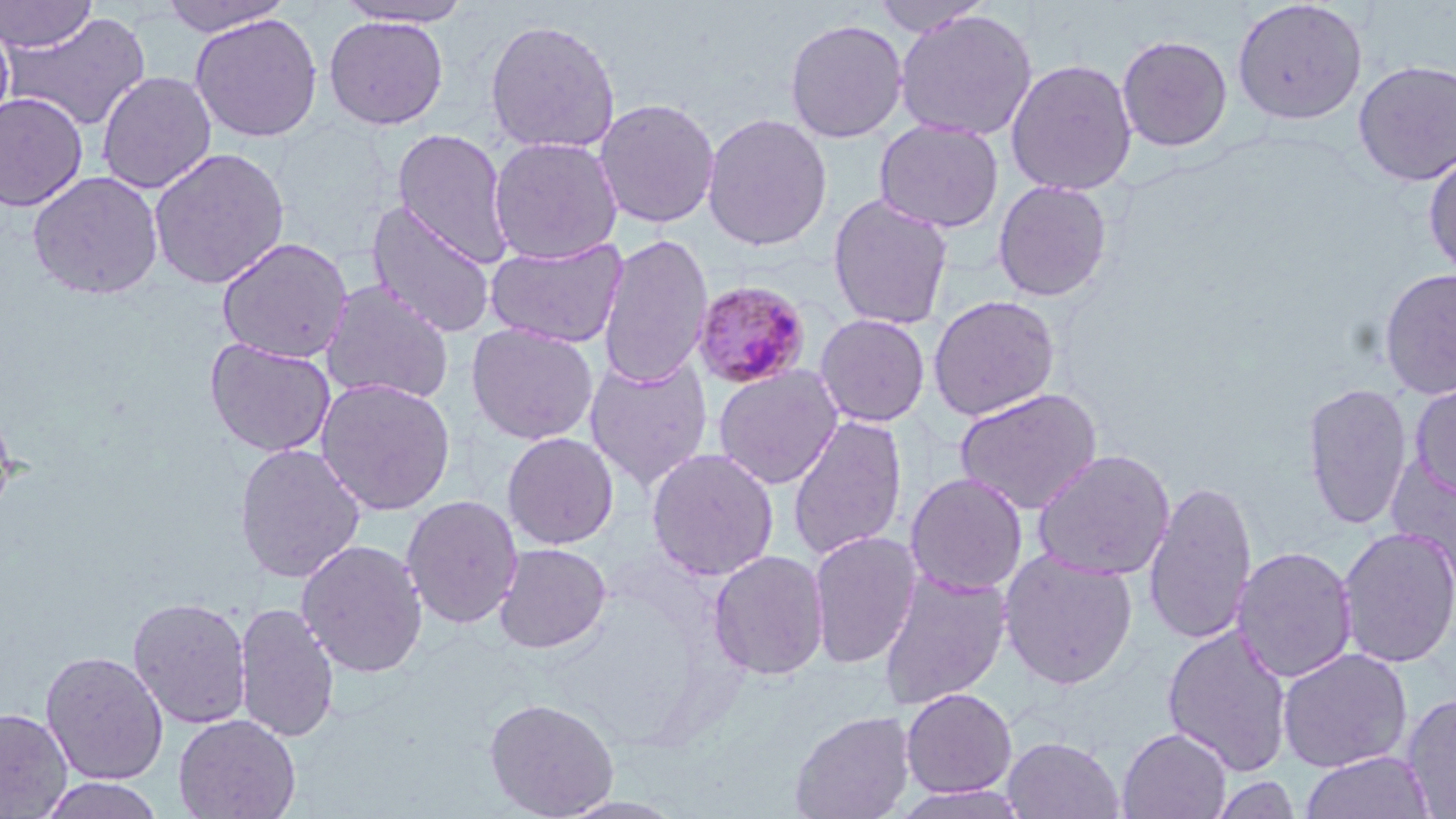
Summary:
  - Coordinate format: approximate bounding boxes as named x1/y1/x2/y2 corners in pixels
  - Uninfected red blood cell locations: (x1=0, y1=0, x2=97, y2=53), (x1=869, y1=0, x2=994, y2=37), (x1=1232, y1=0, x2=1368, y2=125), (x1=158, y1=1, x2=293, y2=36), (x1=332, y1=1, x2=475, y2=28), (x1=893, y1=8, x2=1039, y2=142), (x1=2, y1=11, x2=152, y2=132), (x1=190, y1=13, x2=323, y2=143), (x1=323, y1=15, x2=449, y2=130), (x1=0, y1=16, x2=15, y2=135), (x1=484, y1=17, x2=621, y2=156), (x1=784, y1=18, x2=908, y2=144), (x1=1116, y1=34, x2=1233, y2=152), (x1=1005, y1=58, x2=1138, y2=196), (x1=1352, y1=59, x2=1456, y2=187), (x1=97, y1=71, x2=217, y2=194), (x1=0, y1=92, x2=88, y2=212), (x1=593, y1=97, x2=721, y2=229), (x1=701, y1=112, x2=833, y2=252), (x1=873, y1=118, x2=1004, y2=234), (x1=392, y1=128, x2=514, y2=266), (x1=488, y1=136, x2=623, y2=265), (x1=149, y1=147, x2=290, y2=290), (x1=1423, y1=148, x2=1456, y2=280), (x1=27, y1=171, x2=164, y2=300), (x1=992, y1=179, x2=1113, y2=302), (x1=827, y1=193, x2=954, y2=331), (x1=366, y1=201, x2=498, y2=339), (x1=597, y1=232, x2=713, y2=390), (x1=217, y1=237, x2=353, y2=363), (x1=485, y1=239, x2=628, y2=348), (x1=1378, y1=266, x2=1456, y2=400), (x1=320, y1=281, x2=455, y2=405), (x1=927, y1=294, x2=1061, y2=421), (x1=815, y1=313, x2=931, y2=428), (x1=465, y1=323, x2=598, y2=445), (x1=204, y1=337, x2=336, y2=458), (x1=585, y1=355, x2=714, y2=491), (x1=712, y1=365, x2=844, y2=489), (x1=315, y1=377, x2=456, y2=515), (x1=1409, y1=379, x2=1456, y2=500), (x1=1301, y1=381, x2=1414, y2=531), (x1=953, y1=387, x2=1104, y2=515), (x1=0, y1=398, x2=17, y2=525), (x1=787, y1=414, x2=908, y2=561), (x1=501, y1=432, x2=619, y2=550), (x1=234, y1=442, x2=366, y2=584), (x1=645, y1=448, x2=780, y2=582), (x1=1031, y1=448, x2=1176, y2=581), (x1=1385, y1=456, x2=1456, y2=595), (x1=904, y1=472, x2=1029, y2=596), (x1=1142, y1=479, x2=1259, y2=647), (x1=401, y1=494, x2=523, y2=630), (x1=1337, y1=526, x2=1456, y2=668), (x1=808, y1=530, x2=923, y2=669), (x1=296, y1=539, x2=429, y2=677), (x1=493, y1=542, x2=611, y2=654), (x1=1231, y1=545, x2=1358, y2=684), (x1=707, y1=549, x2=830, y2=680), (x1=998, y1=549, x2=1139, y2=691), (x1=878, y1=570, x2=1013, y2=710), (x1=128, y1=596, x2=252, y2=730), (x1=234, y1=602, x2=340, y2=743), (x1=1161, y1=624, x2=1294, y2=776), (x1=1276, y1=647, x2=1413, y2=773), (x1=40, y1=650, x2=168, y2=786), (x1=900, y1=687, x2=1018, y2=798), (x1=1401, y1=692, x2=1456, y2=818), (x1=483, y1=696, x2=620, y2=819), (x1=0, y1=708, x2=73, y2=818), (x1=790, y1=710, x2=915, y2=819), (x1=173, y1=713, x2=301, y2=819), (x1=1117, y1=727, x2=1232, y2=818), (x1=1001, y1=736, x2=1126, y2=819), (x1=1300, y1=750, x2=1436, y2=819), (x1=1207, y1=774, x2=1303, y2=819), (x1=38, y1=776, x2=166, y2=818)
  - Plasmodium malariae-infected red blood cell locations: (x1=691, y1=280, x2=813, y2=390)
  - Slide-level diagnosis: Plasmodium malariae
  - Image size: 1456×819 pixels
  - Preparation: thin blood film
  - Magnification: 1000x
  - Modality: optical microscopy
  - Stain: May-Grünwald-Giemsa
  - Field of view: one of a larger specimen